Describe the morphology of the erythrocytes.
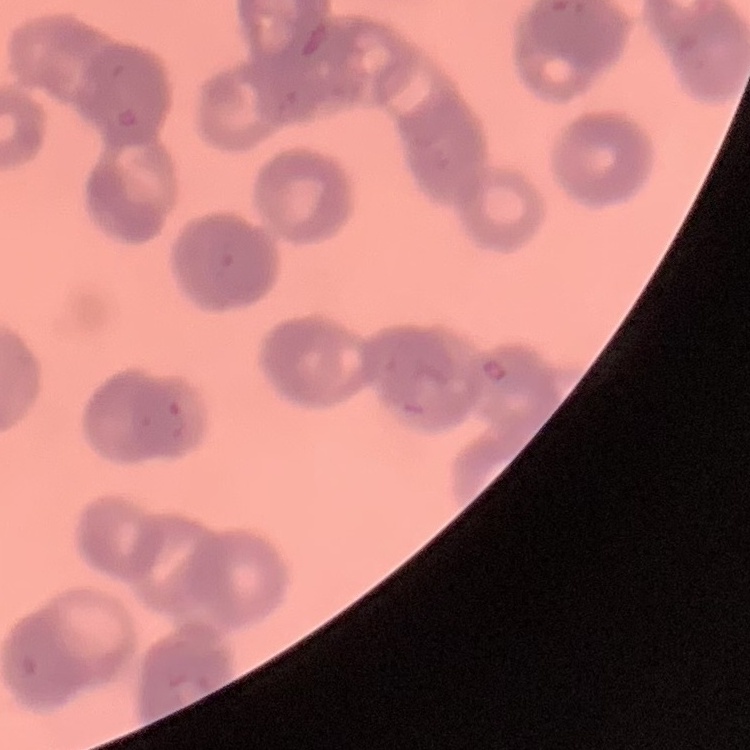
They show rouleaux formation.

One tile cut from a larger photomicrograph. Stained with either Field's or Giemsa. Thin blood smear.